Identify the preparation type.
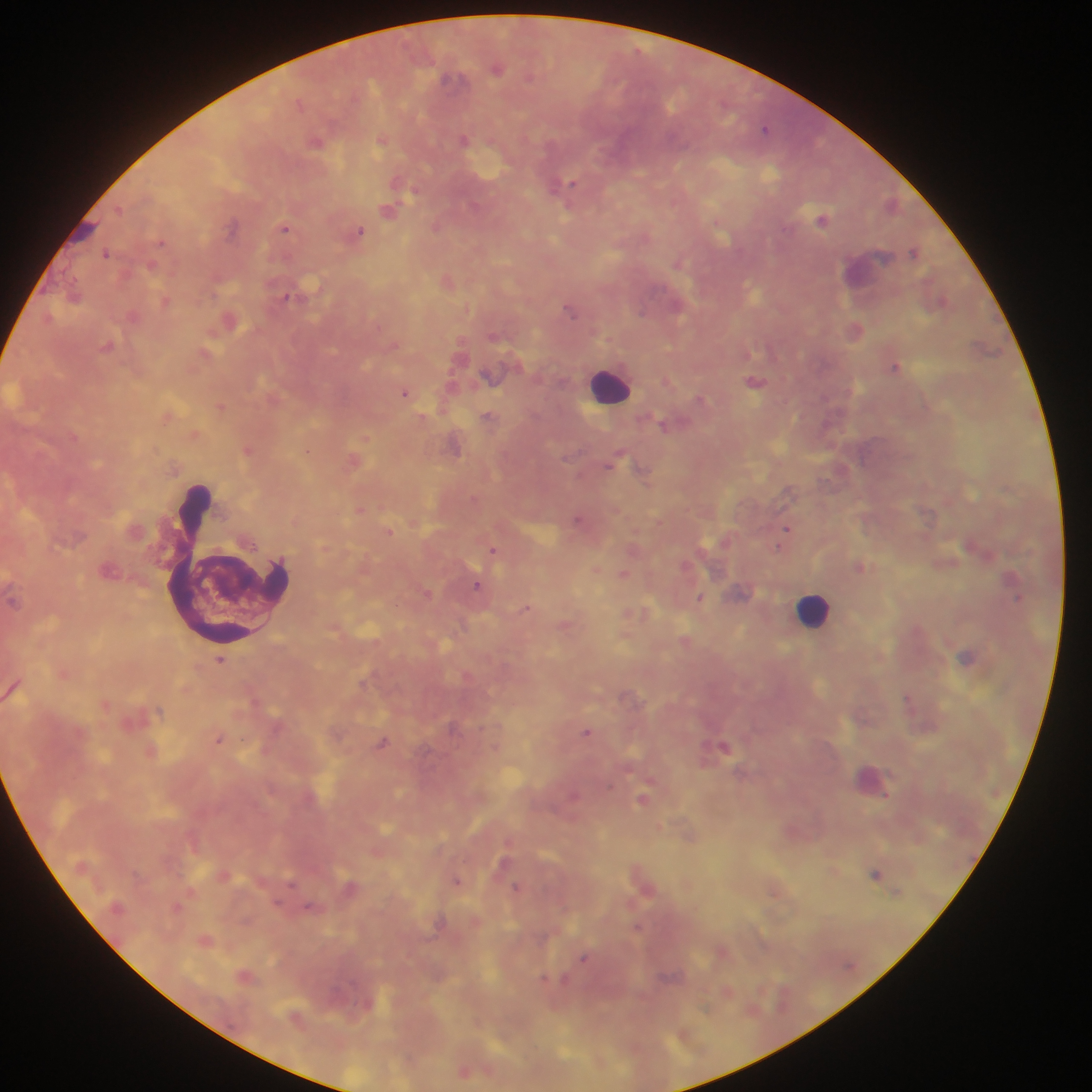
Thick blood film.

Approximate centers as [x, y] in pixels. Leukocyte locations: [610, 385], [815, 609], [871, 780]. Plasmodium parasite locations: [496, 67], [765, 128], [382, 138], [465, 139], [317, 141], [565, 186], [389, 210], [822, 219], [437, 225], [285, 228], [359, 232], [914, 251], [106, 253], [679, 262], [448, 281], [74, 295], [166, 301], [571, 308], [133, 315], [229, 319], [856, 328], [107, 345], [206, 353], [895, 367], [756, 381], [406, 392], [701, 399], [221, 405], [168, 416], [423, 417], [489, 417], [665, 424], [195, 434], [366, 438], [455, 445], [249, 449], [354, 460], [613, 460], [644, 470], [360, 509], [579, 519], [787, 528], [389, 531], [494, 549], [687, 565], [861, 567], [596, 569], [623, 574], [477, 585], [742, 592], [428, 593], [701, 597], [527, 607], [636, 614], [566, 625], [686, 640], [967, 657], [220, 659], [909, 698], [106, 705], [587, 732], [219, 739], [383, 743], [724, 745], [152, 750], [575, 794], [644, 799], [690, 835], [510, 841], [504, 864], [835, 870], [223, 874], [876, 874], [458, 881], [645, 882], [351, 887], [517, 888], [776, 888], [177, 907], [639, 927], [206, 939], [723, 951], [584, 957], [246, 976], [545, 980], [564, 980], [728, 991], [465, 1071]. One field of view. Collected in Ghana. Mobile-phone photograph taken through the microscope. Image is 1092×1092 pixels.